Locate every blood parasite and identify its species.
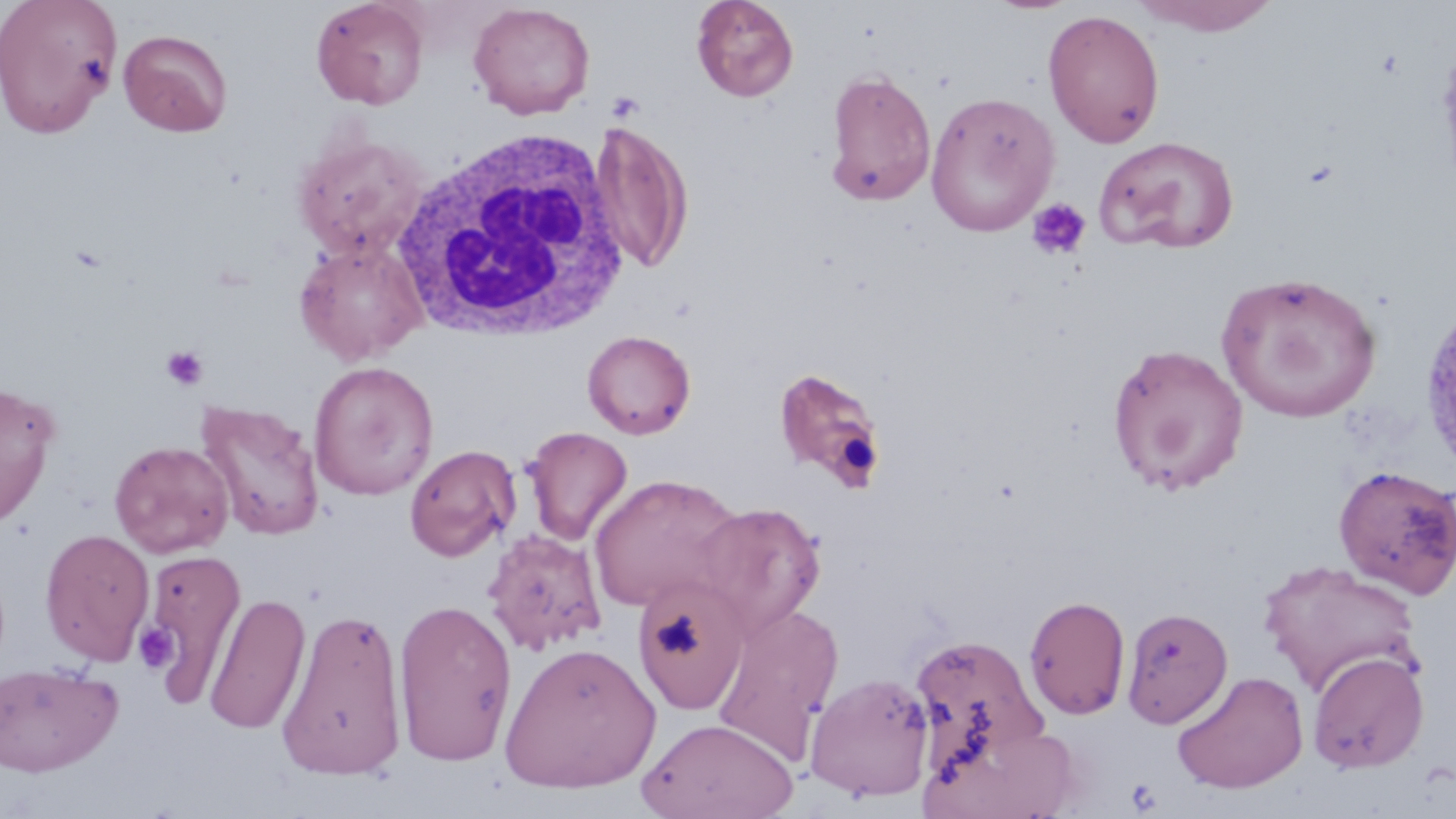
No blood parasites observed.

Approximate bounding boxes as (x1,y1)-(x2,y2) corner pairs in pixels. Uninfected red blood cell locations: (0,0)-(122,139), (311,0)-(429,110), (691,0)-(799,102), (1131,0)-(1283,37), (468,2)-(595,120), (1043,8)-(1165,149), (118,28)-(232,137), (1436,31)-(1456,199), (824,68)-(937,206), (925,91)-(1060,237), (589,121)-(693,274), (293,133)-(430,259), (1093,135)-(1240,255), (294,239)-(429,365), (1216,270)-(1383,422), (1418,296)-(1456,477), (582,329)-(696,439), (1106,342)-(1250,496), (309,361)-(439,501), (774,367)-(888,492), (0,379)-(61,528), (195,399)-(325,541), (522,426)-(633,547), (110,440)-(234,558), (404,444)-(522,562), (1333,465)-(1456,598), (588,473)-(745,613), (693,501)-(826,638), (39,529)-(155,665), (483,529)-(607,655), (141,546)-(246,708), (1257,559)-(1425,699), (631,578)-(750,715), (204,591)-(311,735), (1024,594)-(1131,721), (393,598)-(518,766), (712,601)-(845,763), (277,605)-(409,781), (1121,606)-(1233,728), (909,633)-(1050,776), (499,641)-(660,794), (1307,651)-(1430,774), (0,661)-(123,776), (1171,670)-(1309,794), (805,672)-(934,802), (639,716)-(798,819). White blood cell locations: (391,127)-(632,343). Platelet locations: (1026,197)-(1091,261), (160,346)-(207,391), (135,622)-(178,672), (1126,777)-(1164,814). Slide-level diagnosis: negative for blood parasites. Thin blood film. Image is 1456×819 pixels. 1000x magnification. Optical microscopy. Single field of view. May-Grünwald-Giemsa-stained preparation.